Assess the morphology of the red blood cells.
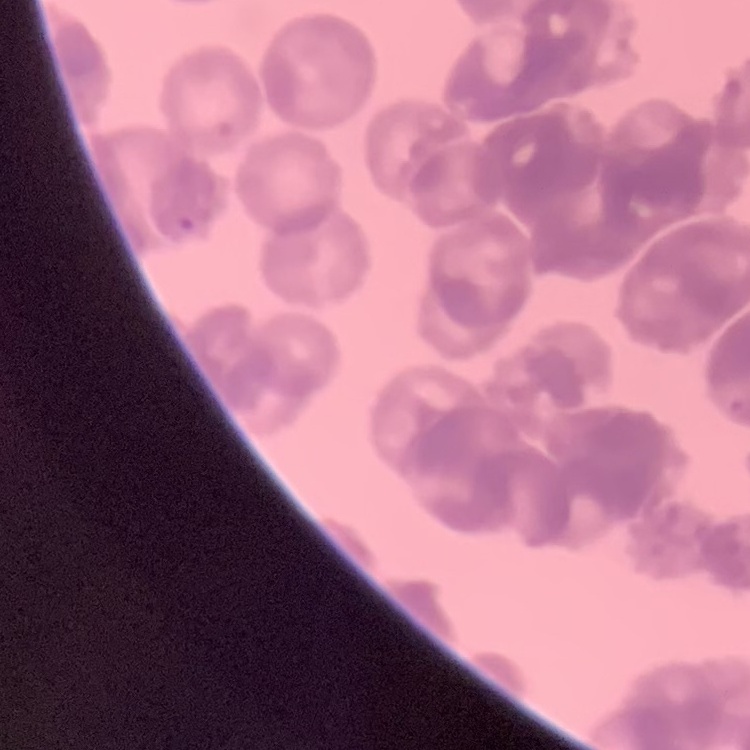
They show rouleaux formation.

One tile cut from a larger photomicrograph. Field's or Giemsa stain. Thin peripheral smear.